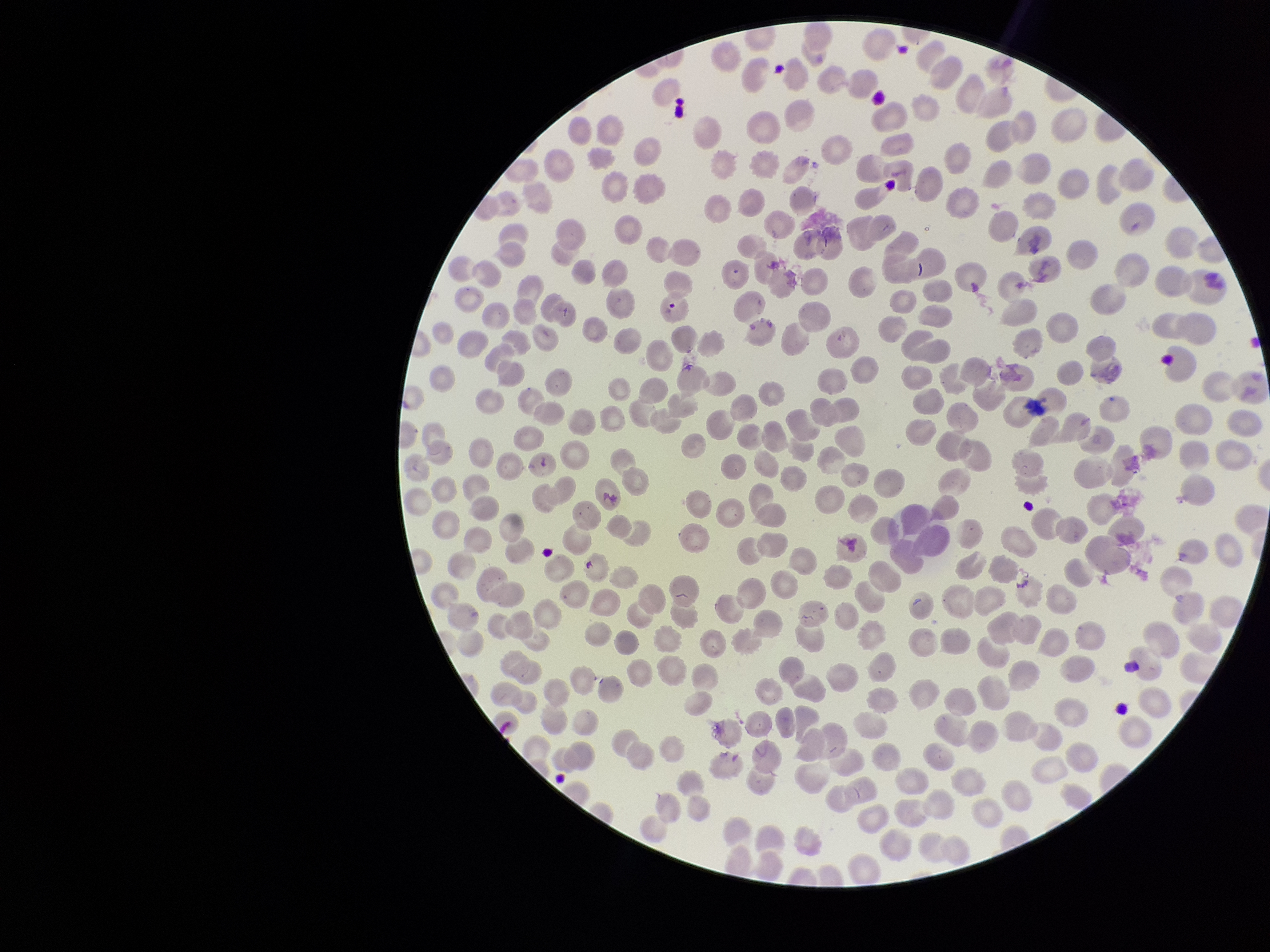
Summary:
  - Parasitized red blood cells: none detected
  - Red blood cell count: 351
  - Preparation: thin smear
  - Species reported for this patient: Plasmodium falciparum
  - Field of view: one from this slide
  - Stain: Giemsa
  - Image size: 1270×952 pixels
  - Patient malaria status: positive
  - Parasitized red blood cell count: 0
  - Capture: smartphone photograph through the microscope eyepiece